Report the malaria status of this cell.
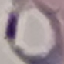
Parasitized.

Automatically extracted cell patch, resized to 64 × 64 pixels. Giemsa stain. Acquired by smartphone through the microscope eyepiece. Thin blood film.